Locate every Plasmodium parasite.
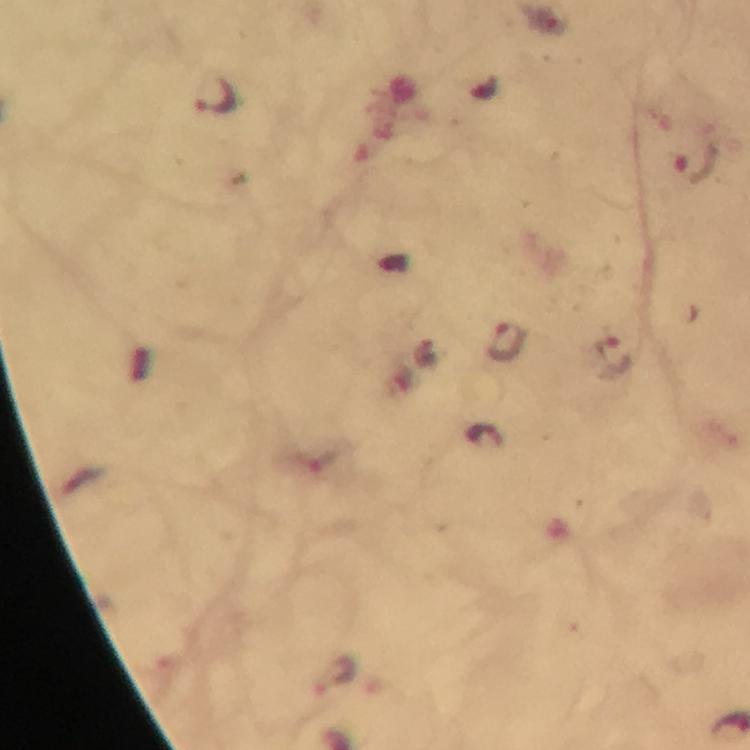
Approximate centers as (x, y) in pixels.
Plasmodium parasites: (214, 97), (695, 168), (508, 340), (613, 357), (490, 438), (334, 675).

Summary:
  - Capture: smartphone photograph through a microscope
  - Preparation: thick smear
  - Immersion oil: applied
  - Stain: Giemsa
  - Cropped from: a single field of view
  - Image size: 750×750 pixels
  - Magnification: 100x
  - Context: from a malaria diagnostic workup